Classify this cell by malaria status.
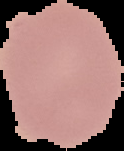

It is uninfected.

{
  "image_size": "124×151 pixels",
  "preparation": "thin blood smear",
  "image_type": "segmented cell region on a black background"
}